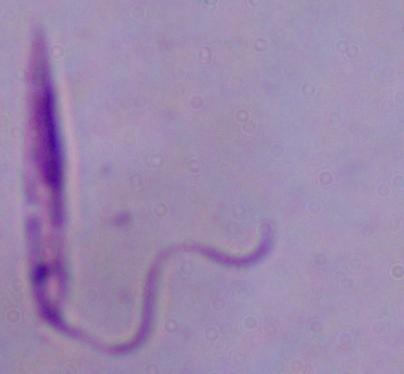

A Leishmania parasite is seen. Captured at 1000x magnification. Micrograph.